Classify this cell by malaria status.
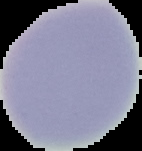
It is uninfected.

Summary:
  - Preparation: thin blood smear
  - Image type: segmented cell region with the area outside set to black
  - Image size: 142×151 pixels